Describe the morphology of the erythrocytes.
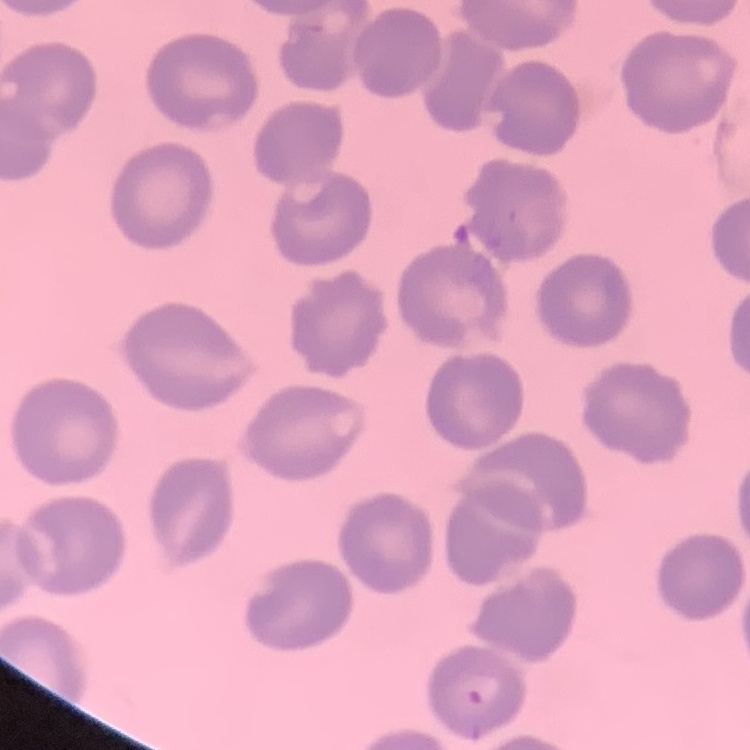

They show no rouleaux formation.

image type = square crop of a larger photomicrograph
stain = Field's or Giemsa
preparation = thin peripheral smear